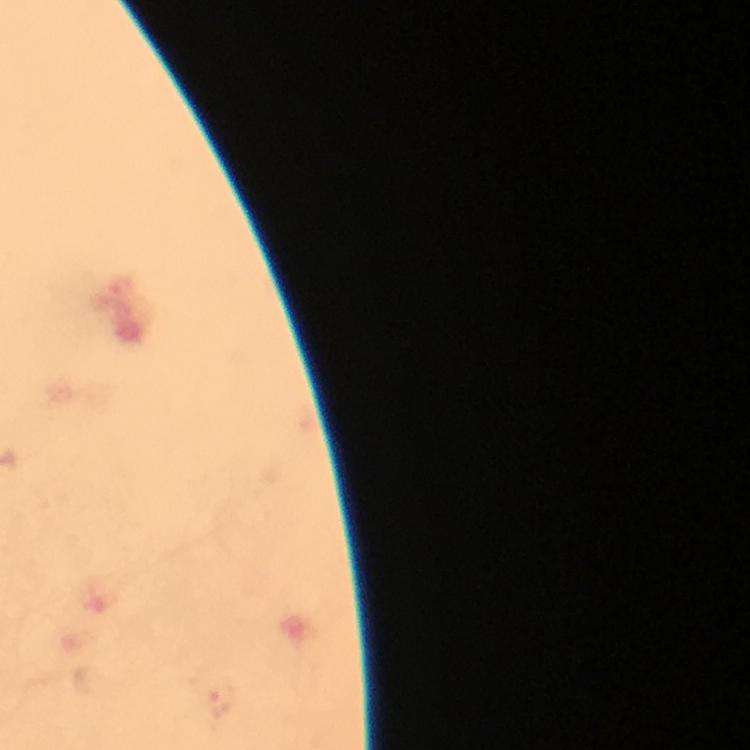
preparation = thick blood film
malaria parasite locations = approximate centers as (x, y) in pixels: (220, 701)
capture = smartphone photograph through a microscope
context = from a malaria diagnostic workup
immersion oil = used
image size = 750×750 pixels
magnification = 100x
stain = Giemsa
cropped from = one field of view